Assess this cell for malaria.
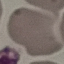
Uninfected.

Automatically extracted cell patch, resized to 64 × 64 pixels. Acquired by smartphone through the microscope eyepiece. Thin blood film. Giemsa stain.